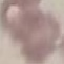

malaria_status: uninfected
preparation: thin blood smear
image_type: automatically extracted cell patch, resized to 64 × 64 pixels
stain: Giemsa
capture: smartphone through the microscope eyepiece